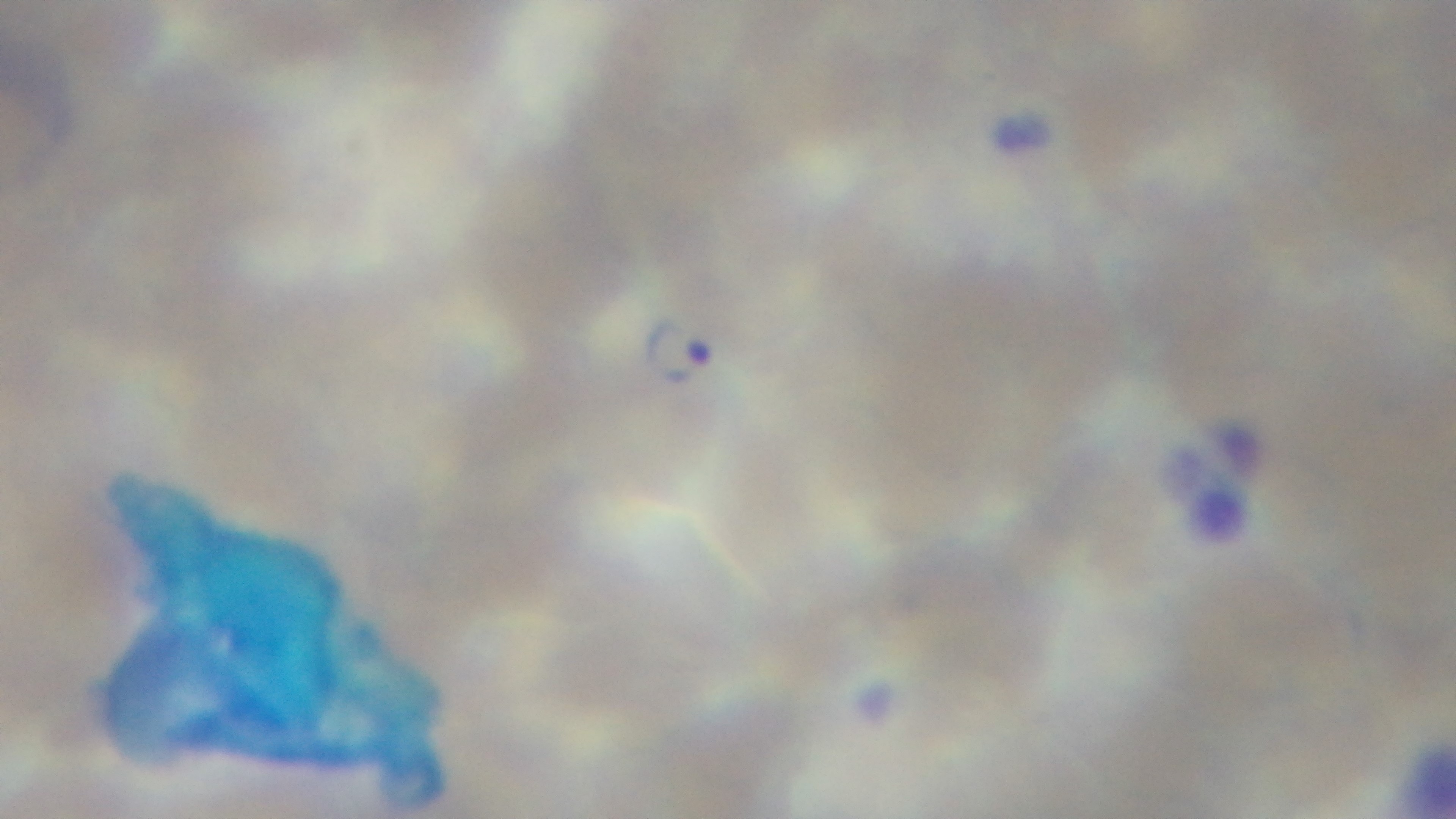 One field from the slide. Malaria status: positive. 100x oil-immersion objective. Mounted 4K digital camera. Giemsa-stained. Photomicrograph. Preparation: thin smear.